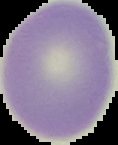

Image is 118×145 pixels. The area outside the segmented cell region is set to black. Result: negative for malaria parasites. From a thin blood smear.